Report the malaria status of this cell.
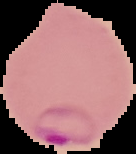

It is parasitized.

Image is 136×154 pixels. Cell region segmented out of the field of view; the surrounding area is masked to black. From a thin blood film.